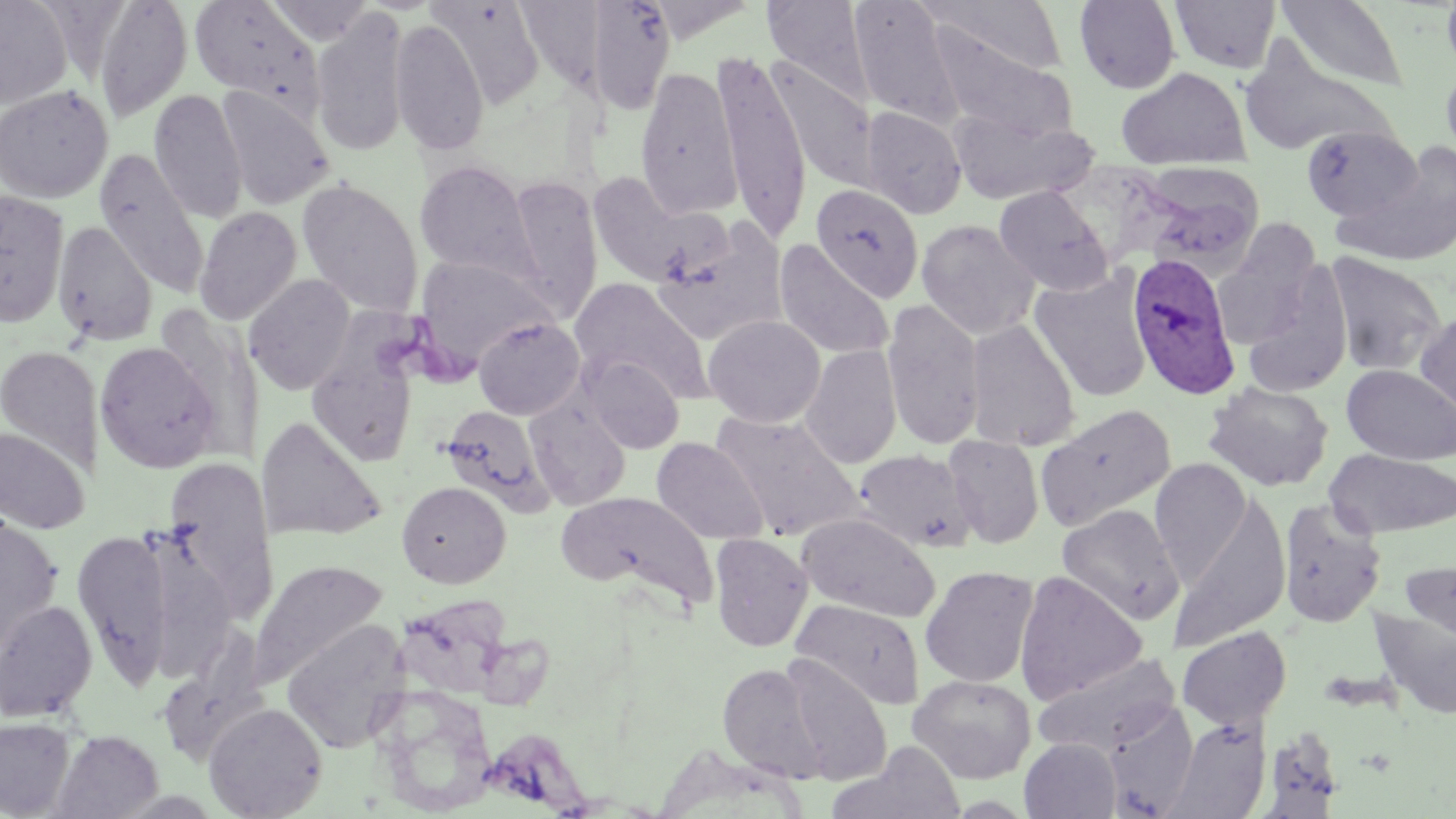
Plasmodium ovale-infected red blood cell locations = approximate bounding boxes as (x1, y1, x2, y2) in pixels: (1128, 252, 1240, 400)
slide-level diagnosis = Plasmodium ovale
magnification = 1000x
modality = light microscopy
uninfected red blood cell locations = approximate bounding boxes as (x1, y1, x2, y2) in pixels: (0, 0, 73, 109), (189, 0, 325, 119), (265, 0, 375, 45), (516, 0, 612, 97), (584, 0, 676, 115), (763, 0, 872, 101), (849, 0, 964, 128), (923, 0, 1068, 77), (1276, 0, 1410, 94), (1441, 0, 1456, 79), (92, 1, 193, 122), (428, 1, 545, 108), (1073, 1, 1181, 94), (1170, 1, 1280, 74), (310, 9, 409, 157), (389, 18, 490, 155), (928, 19, 1075, 143), (1238, 36, 1394, 158), (714, 52, 812, 243), (1440, 55, 1456, 171), (766, 57, 879, 192), (1116, 66, 1250, 168), (635, 67, 743, 217), (0, 84, 114, 203), (216, 87, 334, 210), (148, 89, 248, 223), (860, 106, 967, 219), (949, 109, 1094, 206), (1301, 125, 1424, 224), (1334, 144, 1456, 269), (94, 150, 210, 297), (414, 160, 537, 282), (585, 169, 731, 289), (1142, 170, 1265, 278), (505, 175, 604, 321), (297, 179, 424, 318), (811, 183, 924, 303), (994, 185, 1114, 295), (0, 189, 70, 328), (193, 206, 302, 326), (917, 220, 1039, 339), (53, 221, 157, 345), (652, 222, 789, 346), (1212, 228, 1324, 350), (773, 240, 894, 360), (1324, 252, 1447, 377), (413, 255, 556, 370), (1240, 263, 1352, 398), (1029, 268, 1153, 403), (243, 274, 356, 395), (568, 277, 714, 404), (882, 299, 986, 450), (1415, 308, 1456, 426), (703, 315, 825, 427), (473, 316, 585, 420), (965, 319, 1080, 452), (306, 336, 419, 468), (94, 341, 223, 473), (801, 344, 902, 468), (0, 345, 103, 477), (581, 355, 684, 453), (1342, 364, 1456, 465), (1203, 382, 1334, 492), (525, 398, 631, 510), (1036, 403, 1176, 530), (440, 405, 550, 510), (710, 411, 865, 540), (256, 417, 386, 542), (0, 427, 90, 535), (943, 435, 1043, 548), (651, 437, 769, 544), (854, 448, 975, 553), (1325, 448, 1455, 538), (163, 457, 277, 623), (1150, 457, 1252, 580), (396, 480, 511, 588), (558, 491, 717, 610), (1169, 497, 1293, 651), (1277, 497, 1387, 628), (1058, 505, 1183, 623), (797, 512, 940, 623), (0, 515, 63, 655), (72, 528, 174, 687), (709, 532, 813, 652), (1402, 556, 1456, 645), (250, 559, 388, 686), (921, 565, 1039, 688), (1013, 570, 1147, 705), (791, 598, 925, 710), (0, 600, 98, 722), (1368, 607, 1456, 720), (282, 618, 409, 753), (1177, 626, 1292, 730), (1033, 651, 1182, 756), (780, 656, 892, 784), (718, 662, 826, 781), (908, 674, 1037, 783), (374, 687, 497, 816), (204, 701, 328, 819), (1104, 704, 1200, 818), (0, 716, 75, 818), (1164, 716, 1271, 819), (1259, 727, 1345, 817), (51, 729, 162, 819), (1020, 738, 1121, 819)
image size = 1456×819 pixels
stain = May-Grünwald-Giemsa
preparation = thin blood smear
field of view = single